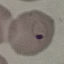
result = malaria parasites detected
stain = Giemsa
capture = smartphone through the microscope eyepiece
preparation = thin blood film
image type = automatically extracted cell patch, resized to 64 × 64 pixels